Report the malaria status of this cell.
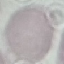
It is uninfected.

{
  "capture": "smartphone camera at the microscope eyepiece",
  "preparation": "thin smear",
  "image_type": "automatically extracted cell patch, resized to 64 × 64 pixels",
  "stain": "Giemsa"
}